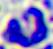
Summary:
  - Magnification: 400x
  - Identification: leukocyte
  - Modality: photomicrograph